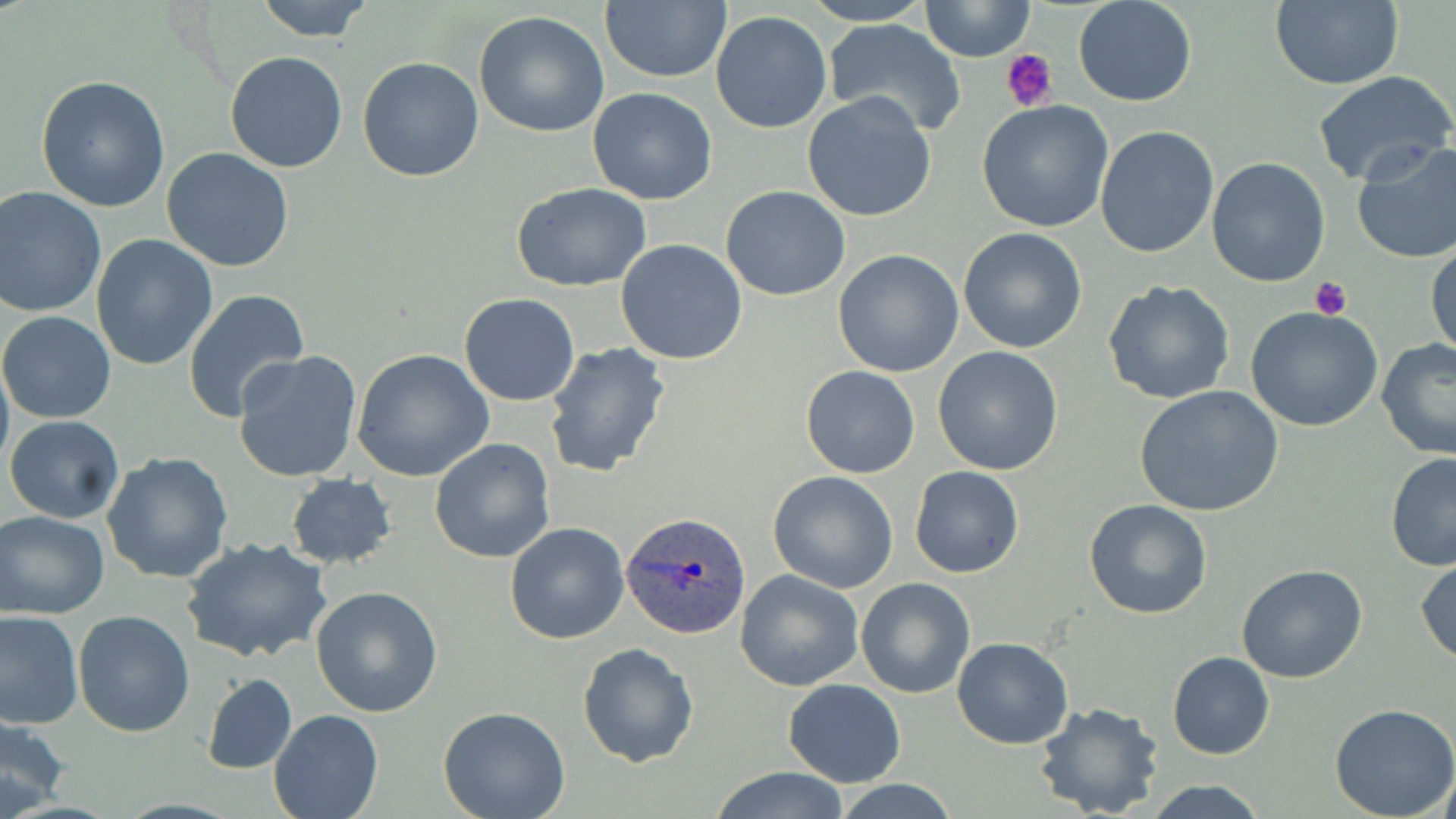

Summary:
  - Coordinate format: approximate bounding boxes as (x1, y1, x2, y2) in pixels
  - Platelet locations: (1000, 47, 1057, 111), (1311, 276, 1351, 320)
  - Uninfected red blood cell locations: (252, 0, 376, 42), (600, 0, 731, 83), (920, 0, 1034, 60), (1073, 0, 1199, 107), (1269, 0, 1404, 89), (795, 1, 940, 26), (711, 10, 832, 133), (473, 11, 611, 139), (821, 19, 967, 137), (223, 51, 348, 174), (357, 56, 483, 182), (1311, 71, 1456, 190), (36, 75, 171, 213), (587, 87, 718, 205), (802, 93, 936, 223), (977, 100, 1113, 232), (1095, 126, 1220, 259), (1349, 139, 1456, 264), (161, 148, 295, 273), (1205, 157, 1331, 288), (512, 182, 654, 292), (721, 184, 851, 302), (0, 187, 106, 320), (957, 227, 1088, 355), (91, 234, 219, 372), (615, 238, 748, 365), (1427, 241, 1456, 365), (832, 249, 966, 378), (1102, 280, 1237, 405), (184, 290, 313, 424), (458, 294, 581, 406), (1244, 306, 1385, 431), (0, 311, 116, 424), (1374, 337, 1456, 460), (544, 341, 672, 481), (352, 347, 494, 482), (932, 347, 1063, 475), (233, 349, 362, 483), (800, 366, 920, 479), (1135, 385, 1286, 518), (6, 416, 125, 524), (430, 438, 556, 564), (102, 451, 234, 585), (1385, 452, 1456, 572), (910, 465, 1024, 577), (767, 470, 899, 593), (284, 474, 398, 569), (1084, 498, 1213, 619), (0, 509, 112, 618), (504, 521, 631, 645), (181, 537, 333, 663), (1414, 554, 1456, 667), (1236, 563, 1368, 683), (734, 569, 864, 693), (856, 577, 976, 699), (311, 587, 443, 717), (73, 609, 194, 737), (1, 610, 83, 728), (952, 636, 1073, 749), (577, 641, 699, 767), (1167, 651, 1275, 760), (202, 673, 297, 773), (784, 679, 906, 787), (1034, 702, 1166, 819), (1330, 703, 1456, 818), (437, 707, 570, 818), (268, 710, 382, 819), (0, 712, 73, 816), (709, 766, 854, 819), (1139, 779, 1271, 818), (832, 780, 963, 817)
  - Plasmodium ovale-infected red blood cell locations: (621, 511, 750, 642)
  - Slide-level diagnosis: Plasmodium ovale
  - Field of view: single
  - Magnification: 1000x
  - Modality: optical microscopy
  - Preparation: thin blood film
  - Image size: 1456×819 pixels
  - Stain: May-Grünwald-Giemsa